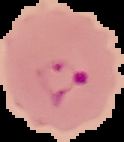

Summary:
  - Image type: segmented cell region on a black background
  - Image size: 124×142 pixels
  - Malaria status: parasitized
  - Preparation: thin blood film